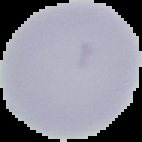

Image is 142×142 pixels. Malaria status: uninfected. From a thin blood film. Cell region segmented out of the field of view; the surrounding area is masked to black.